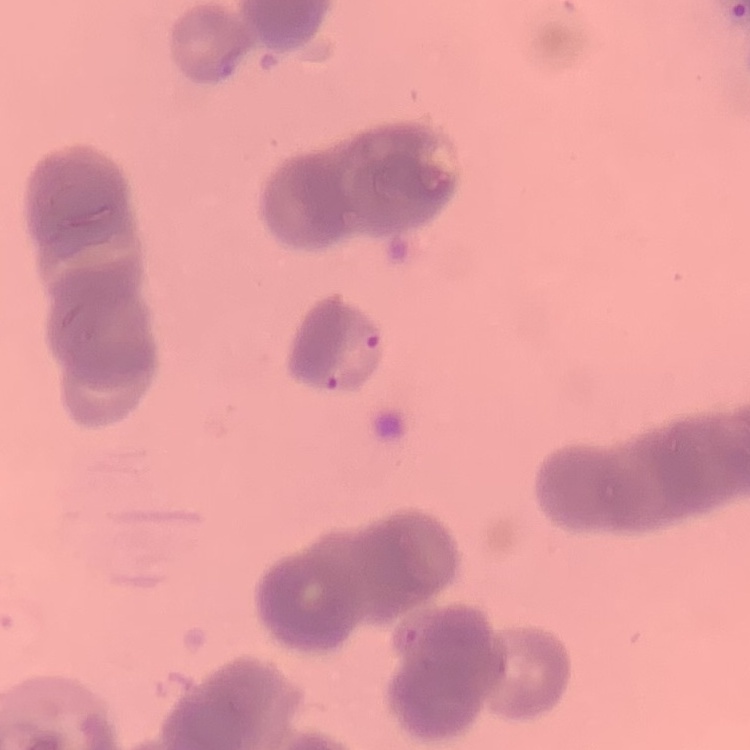
The red blood cells exhibit rouleaux formation. Thin peripheral smear. Field's or Giemsa stain. One tile cut from a larger photomicrograph.